Report the malaria status of this cell.
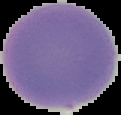
It is uninfected.

Image is 121×115 pixels. From a thin blood smear. Cell region segmented out of the field of view; the surrounding area is masked to black.